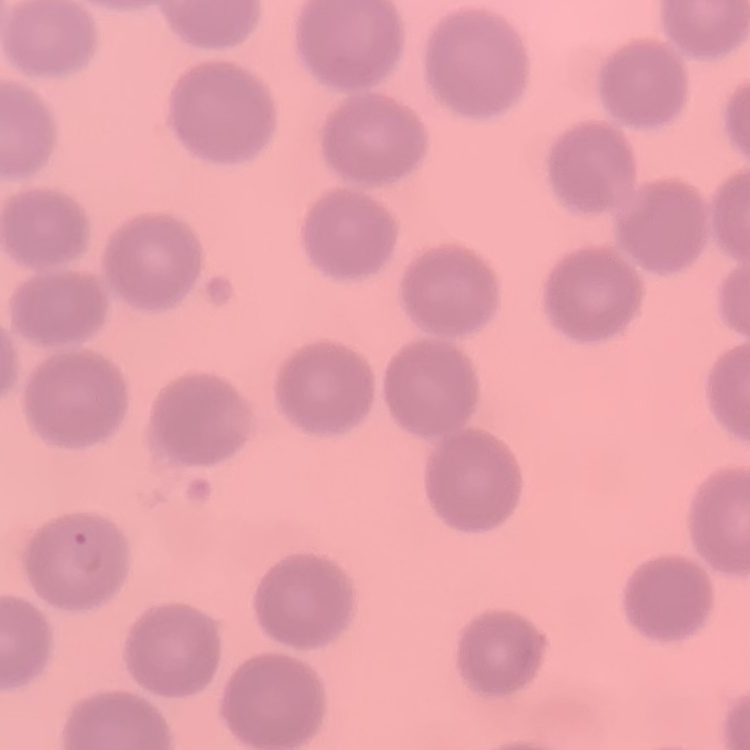

Summary:
  - Red blood cell morphology: no rouleaux formation
  - Preparation: thin blood smear
  - Stain: Field's or Giemsa
  - Image type: one tile cut from a larger photomicrograph